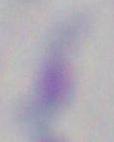
modality: micrograph
magnification: 1000x
identification: Toxoplasma gondii